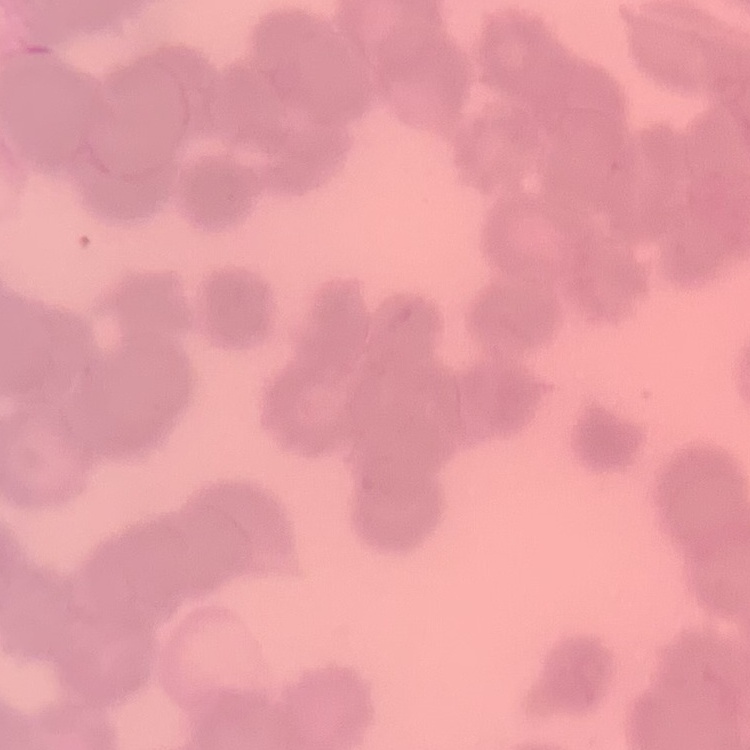

Summary:
  - Red blood cell morphology: rouleaux formation
  - Preparation: thin blood film
  - Stain: Field's or Giemsa
  - Image type: square crop of a larger photomicrograph